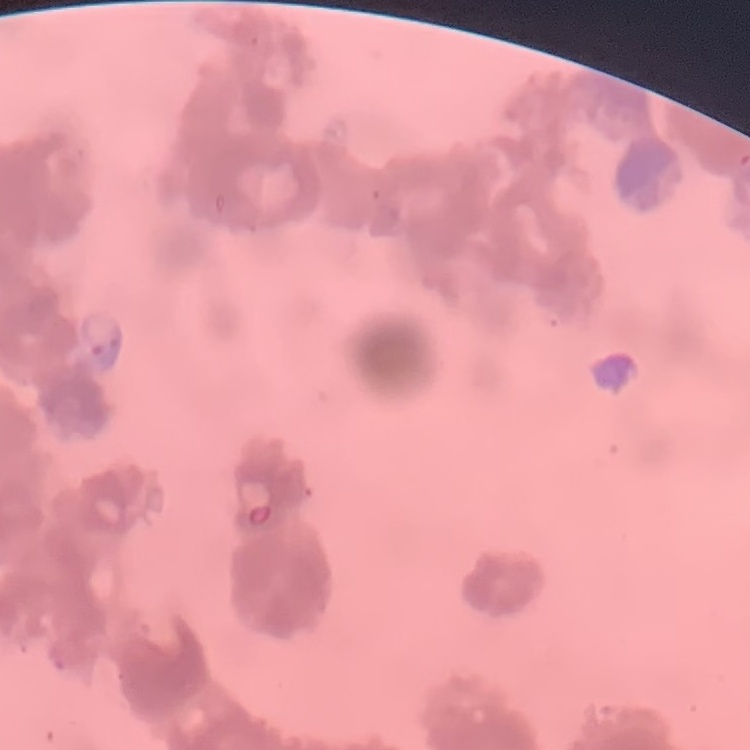
red_blood_cell_morphology: rouleaux formation
image_type: one tile cut from a larger photomicrograph
preparation: thin blood film
stain: Field's or Giemsa